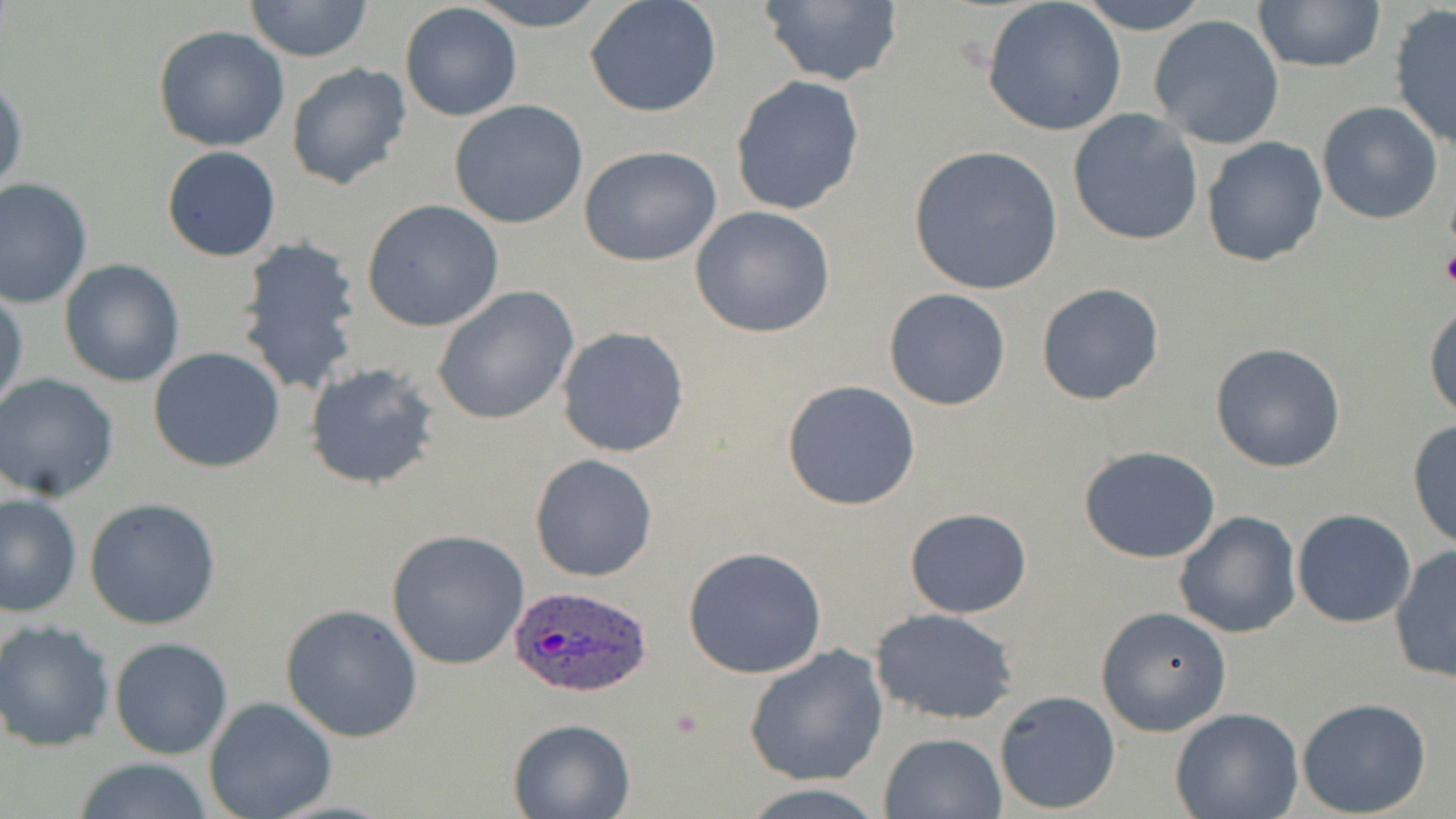 Approximate bounding boxes as (x1,y1)-(x2,y2) corner pairs in pixels. Uninfected red blood cell locations: (242,0)-(376,62), (466,0)-(611,30), (585,0)-(723,118), (751,0)-(907,89), (1074,0)-(1216,35), (1252,0)-(1386,74), (982,2)-(1127,137), (399,3)-(524,121), (1388,6)-(1456,150), (1149,14)-(1285,149), (151,25)-(292,152), (285,62)-(411,192), (0,76)-(27,202), (729,76)-(865,217), (448,100)-(589,230), (1316,101)-(1444,224), (1066,109)-(1205,248), (1200,137)-(1327,267), (909,143)-(1065,296), (579,144)-(723,267), (161,146)-(281,262), (0,178)-(93,307), (361,199)-(504,332), (691,205)-(839,339), (233,233)-(365,396), (59,260)-(185,387), (1036,282)-(1164,405), (432,286)-(580,426), (883,287)-(1012,411), (1,289)-(26,416), (1424,303)-(1456,420), (556,326)-(691,458), (1209,342)-(1346,472), (147,345)-(286,472), (304,361)-(445,489), (0,374)-(120,501), (781,380)-(921,510), (1409,420)-(1456,551), (1079,446)-(1222,564), (529,453)-(659,581), (1,491)-(82,617), (85,497)-(222,631), (904,507)-(1032,619), (1292,510)-(1417,627), (1173,511)-(1302,639), (386,528)-(530,671), (1389,545)-(1456,686), (682,546)-(827,679), (281,604)-(422,742), (1096,604)-(1234,737), (869,609)-(1021,724), (0,621)-(117,752), (109,636)-(233,758), (744,644)-(888,786), (993,689)-(1122,814), (203,696)-(337,819), (1297,697)-(1432,817), (1170,708)-(1303,819), (506,717)-(636,819), (879,732)-(1006,818), (68,758)-(218,818), (739,783)-(889,817). Platelet locations: (1440,248)-(1456,291). Plasmodium ovale-infected red blood cell locations: (508,583)-(655,697). Slide-level diagnosis: Plasmodium ovale. Single field of view. Light microscopy. Thin blood film. Captured at 1000x magnification. May-Grünwald-Giemsa-stained preparation. Image is 1456×819 pixels.